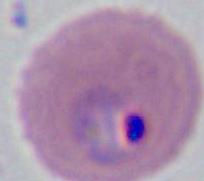

A Plasmodium parasite is shown. Captured at either 400x or 1000x magnification. Photomicrograph.